Assess this cell for malaria.
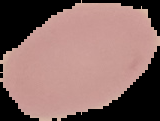
Uninfected.

image type = segmented cell region on a black background
image size = 160×121 pixels
preparation = thin blood smear